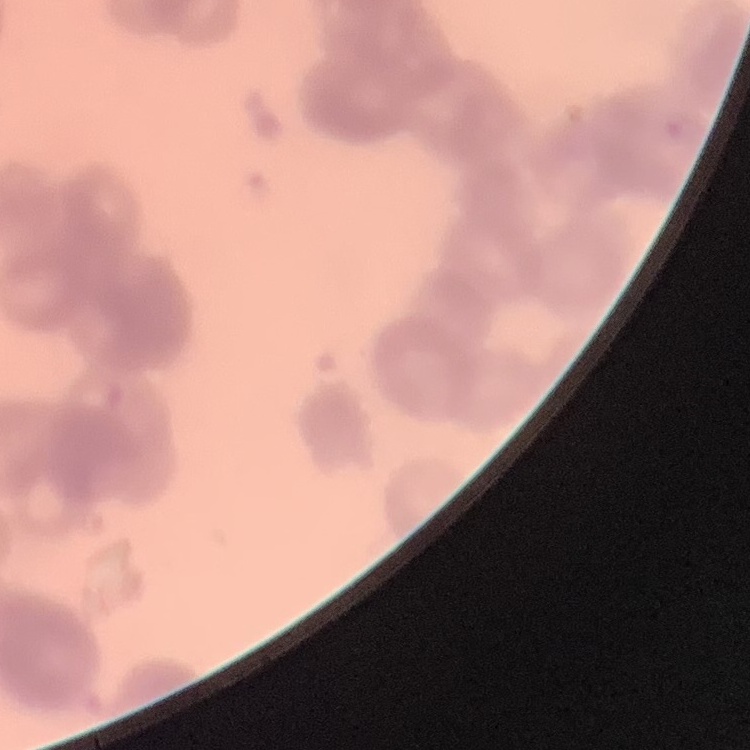

Summary:
  - Erythrocyte morphology: rouleaux formation
  - Image type: one tile cut from a larger photomicrograph
  - Preparation: thin blood smear
  - Stain: Field's or Giemsa